Point out each Plasmodium parasite.
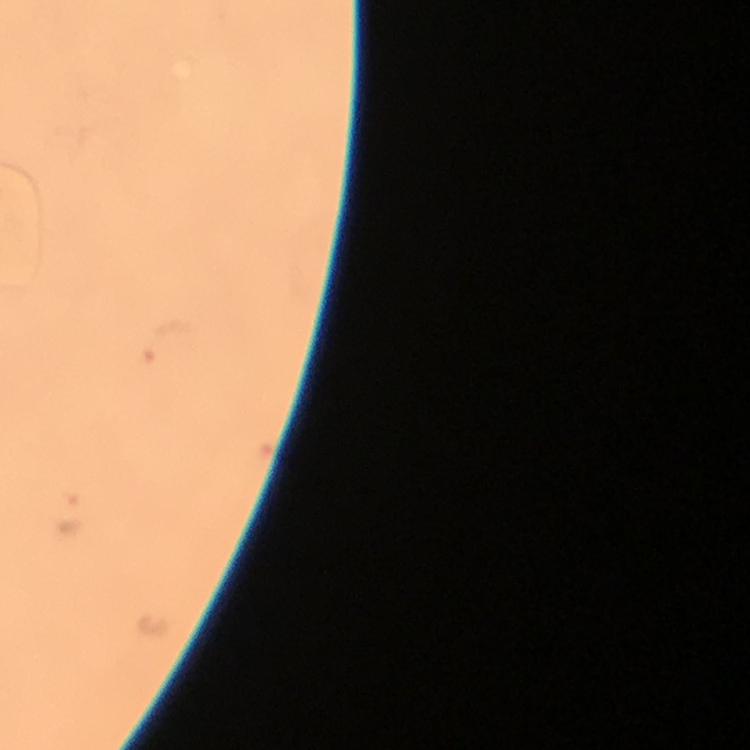

Approximate object centers, in pixels from the top-left corner.
Plasmodium parasites: (x=167, y=342), (x=67, y=513).

capture: smartphone mounted on the microscope
immersion_oil: applied
context: from a diagnostic examination for malaria
image_size: 750×750 pixels
cropped_from: a single field of view
magnification: 100x
stain: Giemsa
preparation: thick blood smear